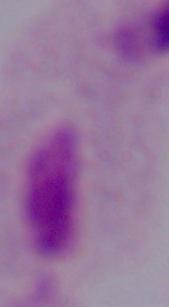
1000x magnification. Micrograph. A trichomonad is seen.